Assess this cell for malaria.
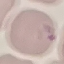

It is parasitized.

{
  "capture": "smartphone camera at the microscope eyepiece",
  "image_type": "automatically extracted cell patch, resized to 64 × 64 pixels",
  "preparation": "thin smear",
  "stain": "Giemsa"
}